Report the malaria status.
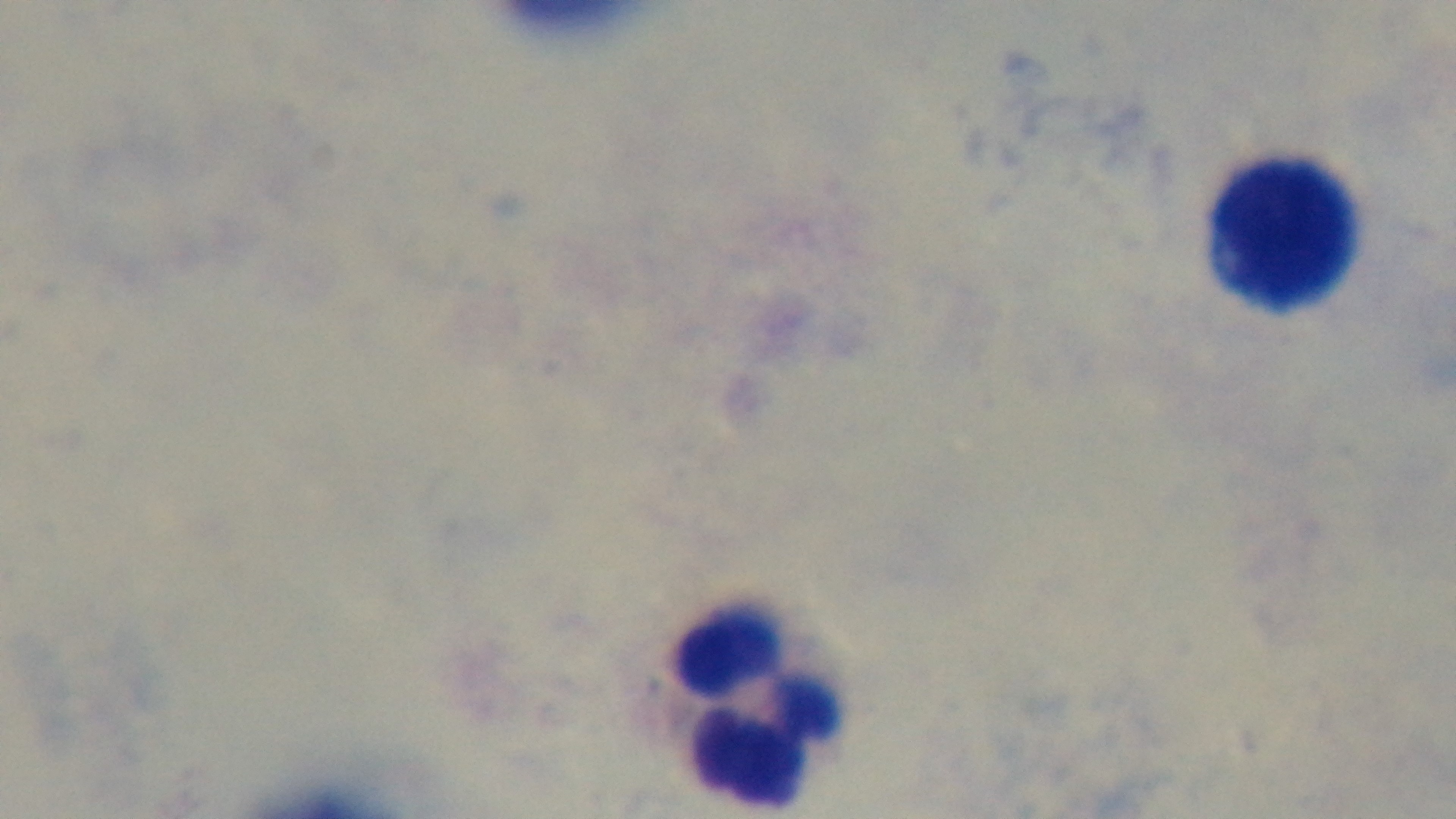

Uninfected.

Summary:
  - Stain: Giemsa
  - Preparation: thick smear
  - Capture: mounted 4K digital camera
  - Modality: light microscopy
  - Objective: 100x oil immersion
  - Field of view: single